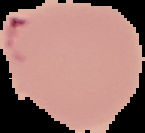 Segmented cell region on a black background. From a thin blood smear. Image is 145×133 pixels. Malaria status: parasitized.